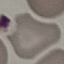

Summary:
  - Result: negative for malaria parasites
  - Capture: smartphone through the microscope eyepiece
  - Image type: cell patch, automatically extracted from a larger field of view and resized to 64 × 64 pixels
  - Preparation: thin smear
  - Stain: Giemsa